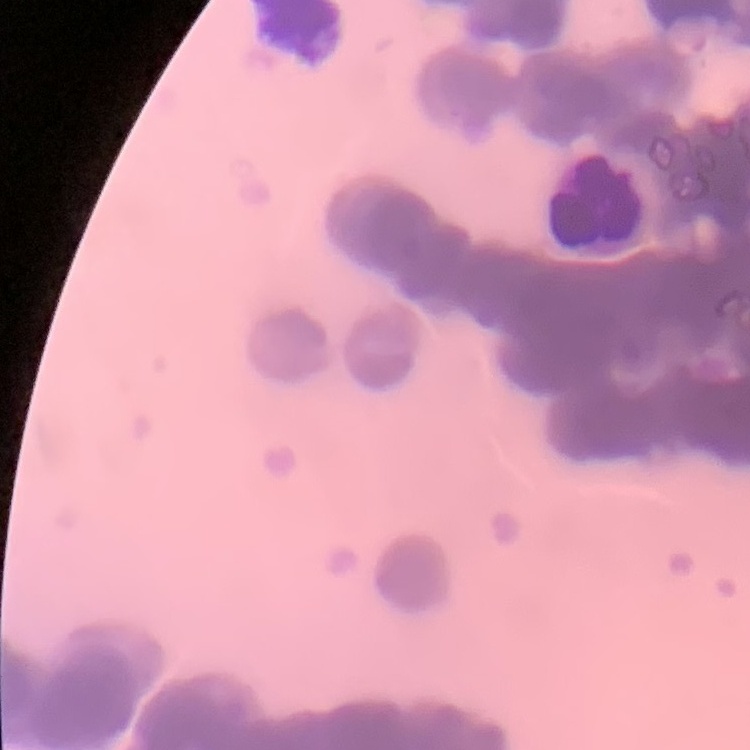
The erythrocytes show rouleaux formation. One tile cut from a larger photomicrograph. Thin blood film. Field's or Giemsa stain.